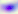

Summary:
  - Magnification: 400x
  - Identification: Toxoplasma gondii
  - Modality: micrograph